Assess for malaria.
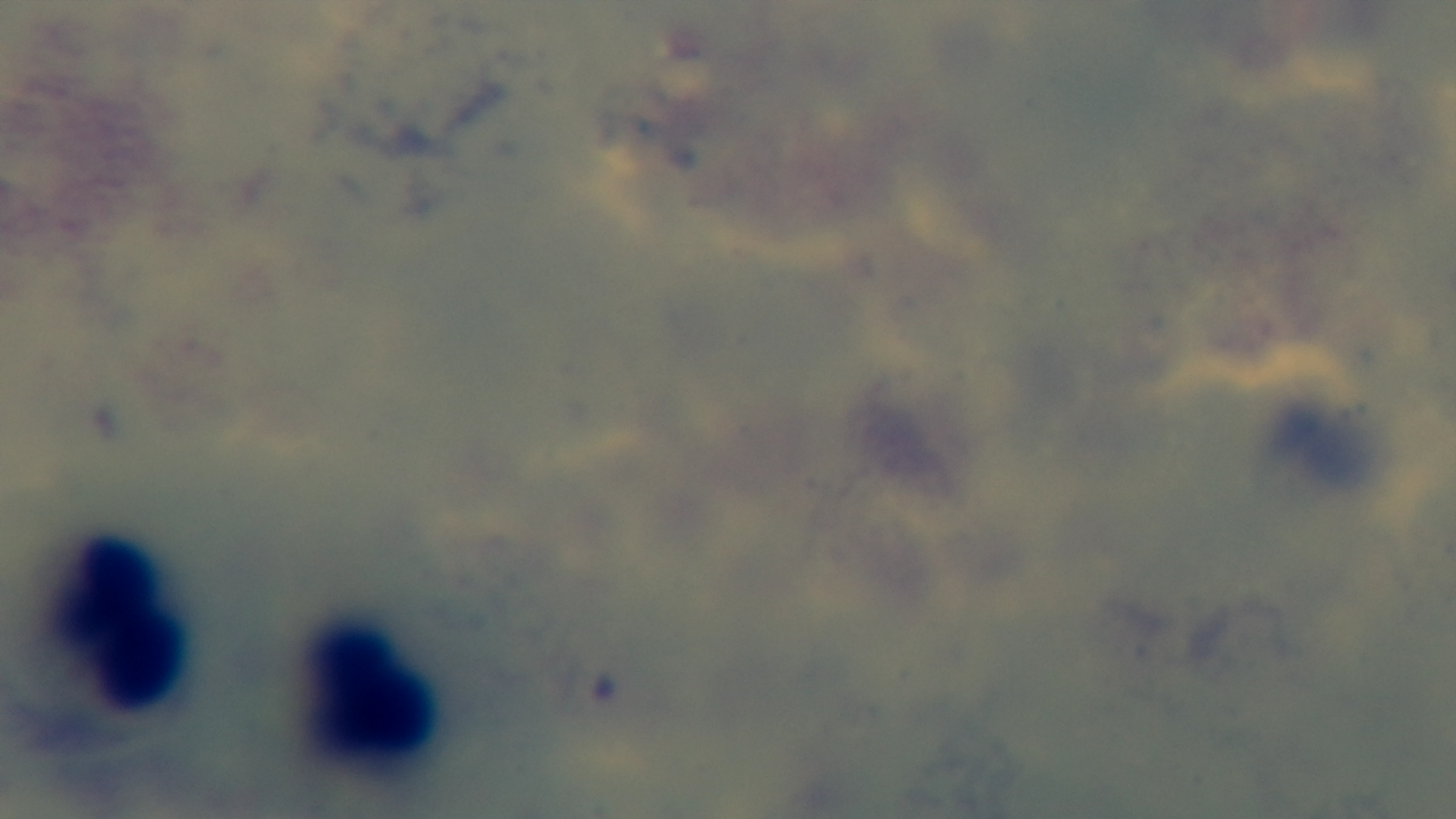
It is uninfected.

Summary:
  - Field of view: one from the slide
  - Capture: mounted 4K digital camera
  - Stain: Giemsa
  - Objective: 100x oil immersion
  - Modality: light microscopy
  - Preparation: thick smear